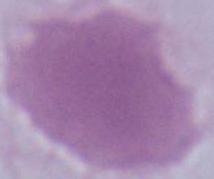

Summary:
  - Identification: red blood cell
  - Magnification: 1000x
  - Modality: micrograph